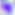
{
  "identification": "Toxoplasma gondii",
  "modality": "micrograph",
  "magnification": "400x"
}